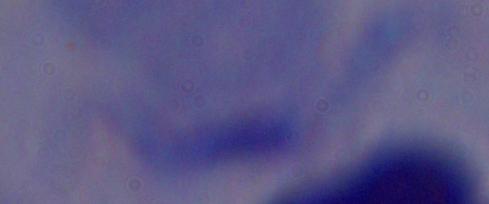
identification = trypanosome
magnification = 1000x
modality = micrograph